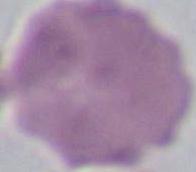
Summary:
  - Identification: red blood cell
  - Magnification: 1000x
  - Modality: micrograph